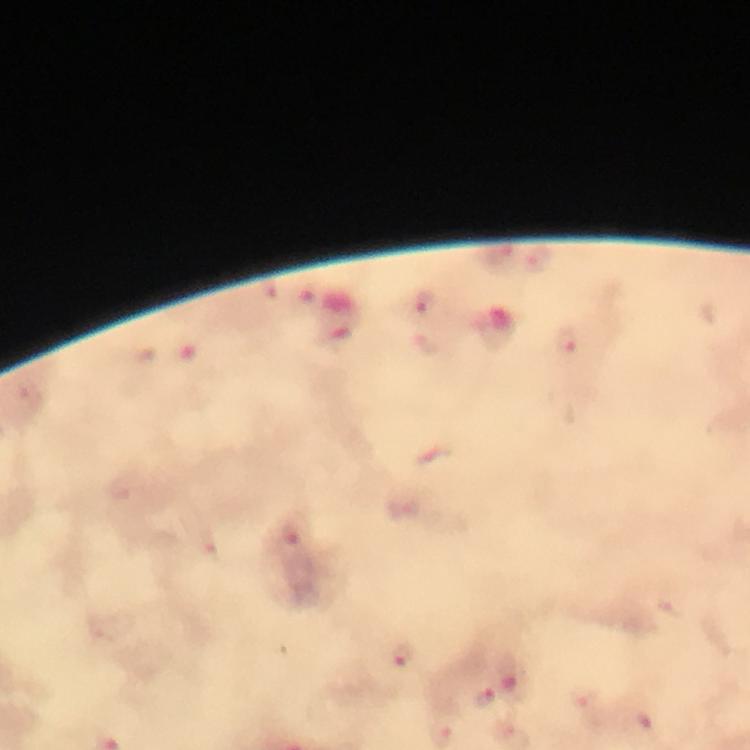
{
  "preparation": "thick smear",
  "immersion_oil": "applied",
  "cropped_from": "a single field of view",
  "stain": "Giemsa",
  "image_size": "750×750 pixels",
  "malaria_parasite_locations": "approximate centers as {x, y} in pixels: {540, 261}, {425, 303}, {566, 338}, {404, 656}, {512, 676}, {584, 697}, {484, 699}",
  "context": "from a malaria diagnostic workup",
  "capture": "smartphone mounted on the microscope",
  "magnification": "100x"
}